Comment on the morphology of the erythrocytes.
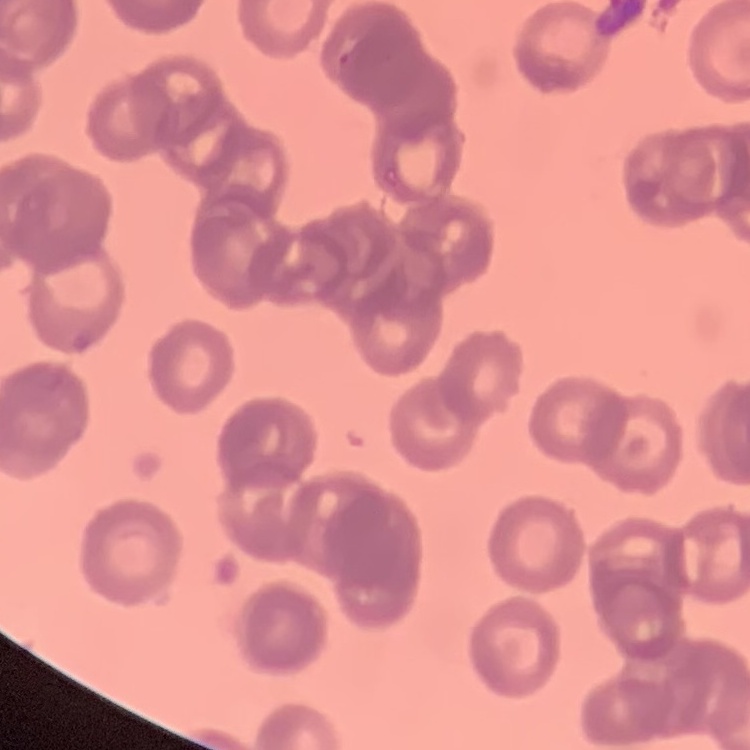
Rouleaux formation.

Summary:
  - Preparation: thin blood smear
  - Image type: one tile cut from a larger photomicrograph
  - Stain: Field's or Giemsa